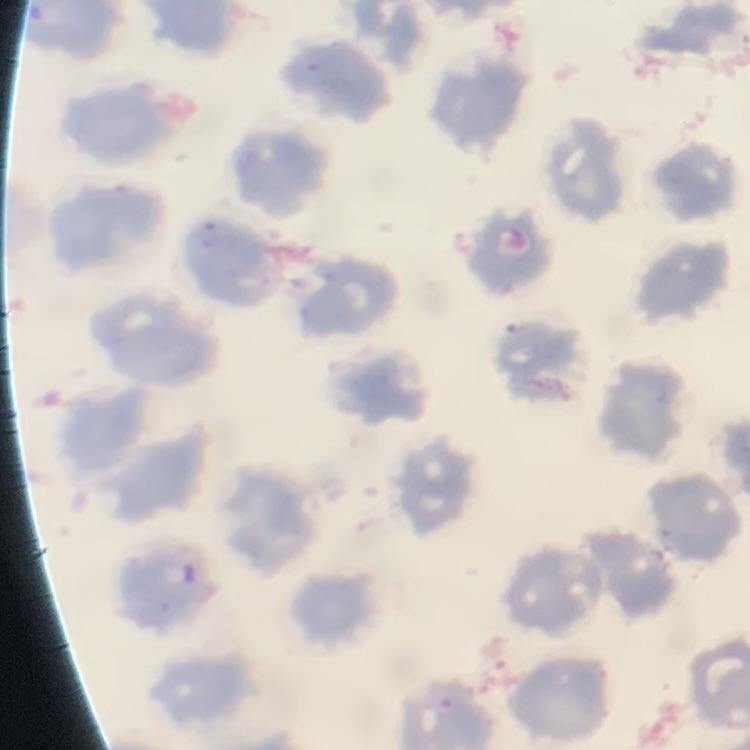

erythrocyte morphology = no rouleaux formation
stain = Field's or Giemsa
preparation = thin blood film
image type = one tile cut from a larger photomicrograph